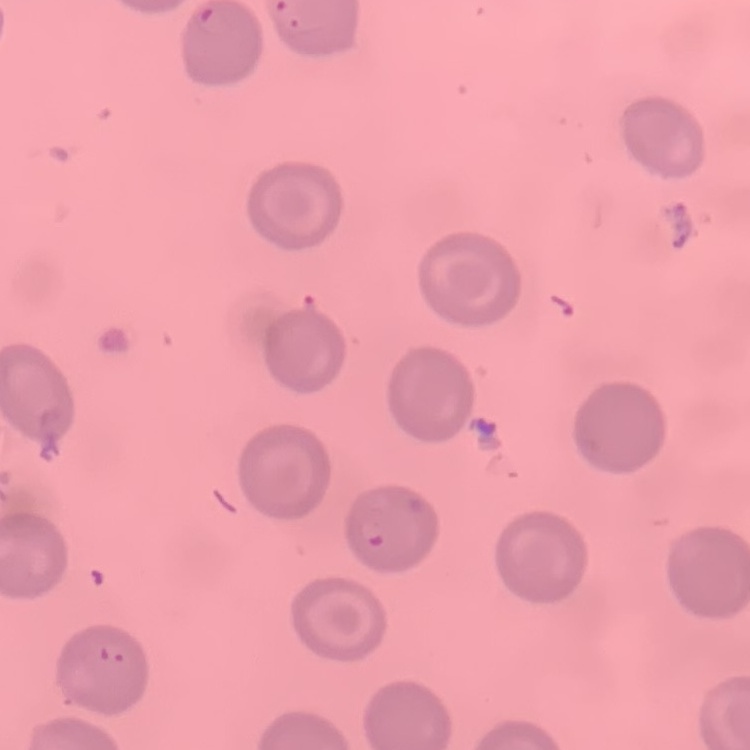

Summary:
  - Red blood cell morphology: no rouleaux formation
  - Preparation: thin peripheral smear
  - Image type: square crop of a larger photomicrograph
  - Stain: Field's or Giemsa